Name the blood parasite species.
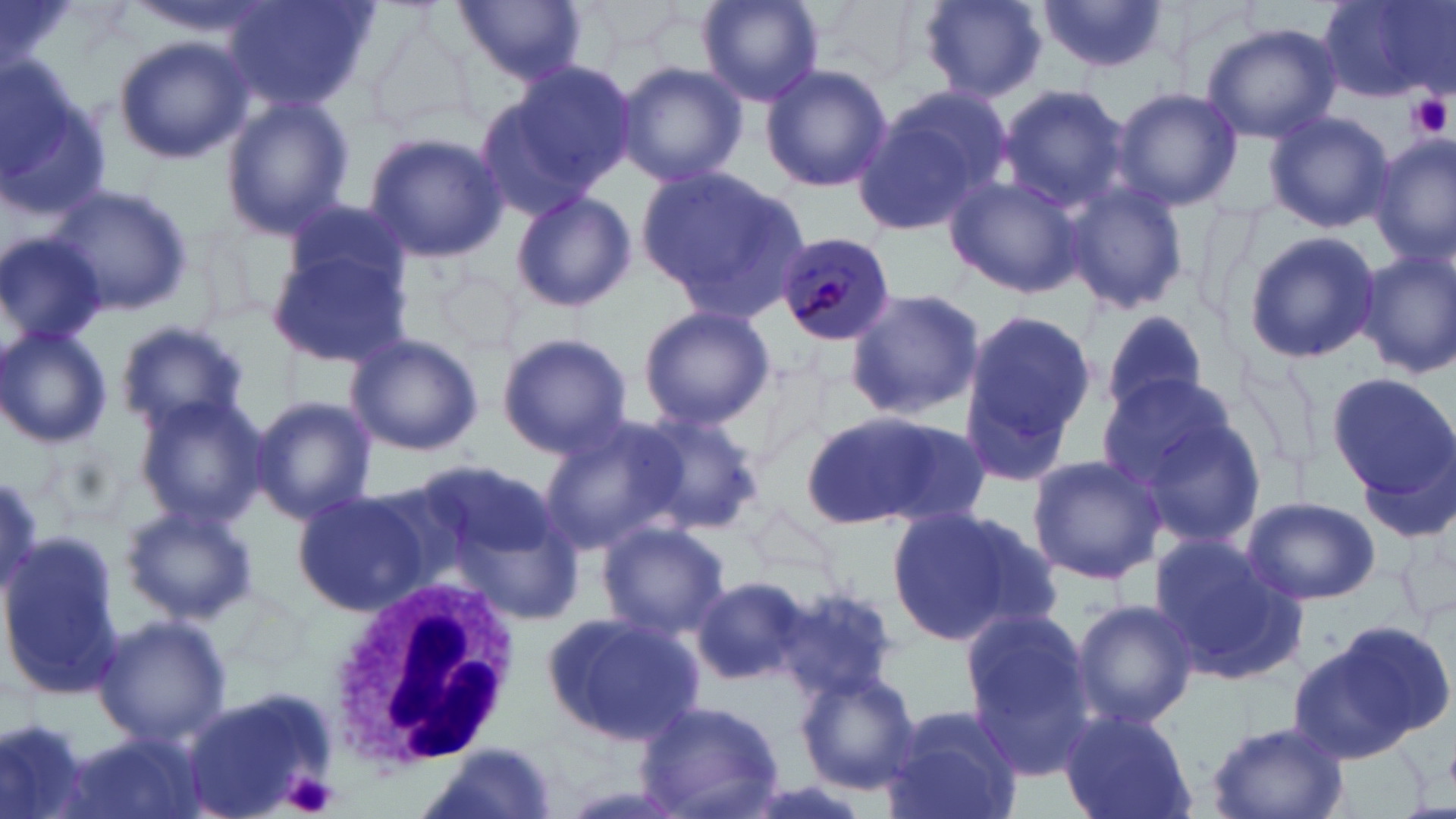
Plasmodium malariae.

Summary:
  - Coordinate format: approximate bounding boxes as (x1, y1, x2, y2) in pixels
  - Plasmodium malariae-infected red blood cell locations: (775, 230, 899, 349)
  - Uninfected red blood cell locations: (223, 0, 376, 113), (453, 0, 588, 86), (697, 0, 824, 107), (814, 0, 932, 85), (914, 0, 1048, 103), (1038, 0, 1173, 72), (1316, 0, 1450, 104), (125, 1, 273, 40), (367, 17, 474, 137), (1200, 22, 1340, 143), (112, 34, 252, 166), (615, 60, 748, 188), (760, 63, 892, 193), (476, 65, 636, 216), (1, 66, 108, 224), (993, 84, 1131, 213), (858, 87, 1015, 235), (1110, 87, 1243, 211), (221, 95, 355, 239), (1263, 110, 1393, 234), (364, 130, 509, 262), (1370, 136, 1455, 268), (639, 164, 808, 318), (943, 173, 1083, 298), (1057, 179, 1191, 316), (48, 184, 194, 319), (511, 189, 635, 313), (1193, 196, 1269, 326), (283, 197, 411, 300), (1241, 231, 1383, 363), (0, 235, 110, 346), (265, 247, 410, 369), (1358, 249, 1456, 380), (434, 269, 520, 358), (843, 286, 986, 421), (636, 305, 775, 429), (956, 306, 1100, 482), (1098, 308, 1210, 417), (114, 318, 252, 435), (0, 325, 112, 451), (496, 332, 633, 460), (344, 333, 483, 457), (1326, 370, 1453, 501), (1102, 380, 1266, 540), (132, 395, 270, 530), (251, 396, 377, 525), (799, 407, 983, 535), (633, 410, 765, 536), (538, 413, 685, 558), (1026, 454, 1166, 585), (433, 470, 587, 630), (291, 489, 424, 613), (1240, 495, 1382, 605), (749, 504, 846, 593), (121, 505, 257, 624), (887, 505, 1055, 648), (595, 520, 731, 641), (0, 535, 125, 700), (1150, 536, 1307, 685), (691, 576, 810, 685), (772, 585, 902, 702), (1069, 599, 1199, 727), (540, 608, 706, 746), (959, 609, 1098, 765), (94, 614, 231, 749), (1291, 624, 1451, 763), (797, 669, 923, 793), (181, 689, 334, 819), (637, 699, 789, 819), (874, 703, 1026, 819), (0, 710, 95, 816), (1057, 710, 1198, 819), (1203, 719, 1352, 819), (60, 734, 209, 819), (422, 744, 562, 818)
  - White blood cell locations: (326, 575, 521, 767)
  - Platelet locations: (1409, 94, 1453, 139), (284, 772, 341, 818)
  - Magnification: 1000x
  - Image size: 1456×819 pixels
  - Modality: light microscopy
  - Stain: May-Grünwald-Giemsa
  - Preparation: thin blood smear
  - Field of view: one of a larger specimen